Assess this cell for malaria.
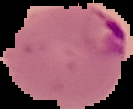

It is parasitized.

Summary:
  - Image size: 133×109 pixels
  - Preparation: thin blood smear
  - Image type: cell region segmented out of the field of view; surrounding area masked to black